Assess this cell for malaria.
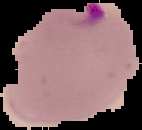
Parasitized.

From a thin blood film. Image is 142×130 pixels. Cell region segmented out of the field of view; the surrounding area is masked to black.